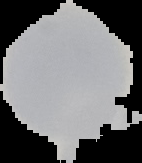
image size = 142×163 pixels
malaria status = uninfected
preparation = thin blood film
image type = cell region segmented out of the field of view; surrounding area masked to black